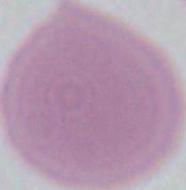
{
  "modality": "micrograph",
  "identification": "erythrocyte",
  "magnification": "1000x"
}